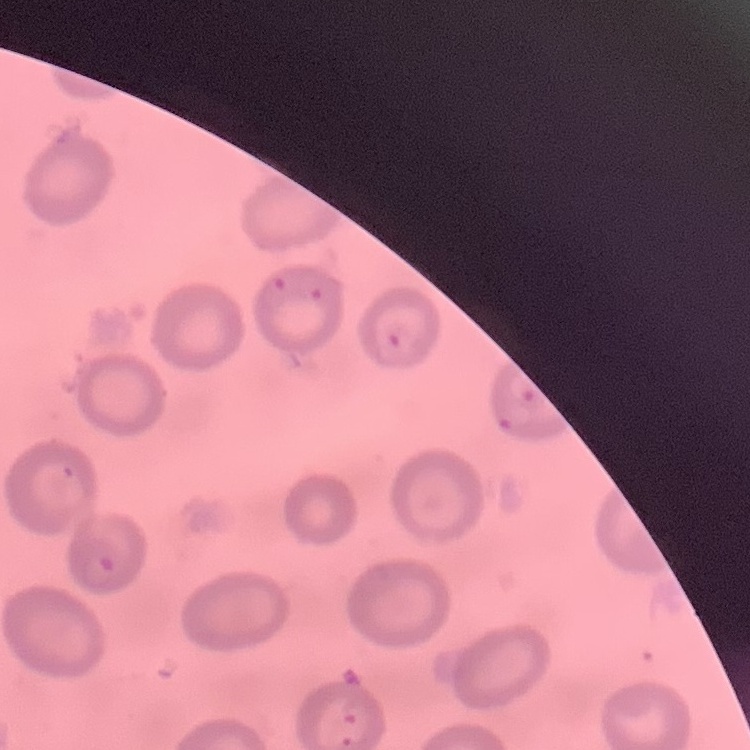

erythrocyte morphology = no rouleaux formation
preparation = thin blood smear
image type = square crop of a larger photomicrograph
stain = Field's or Giemsa